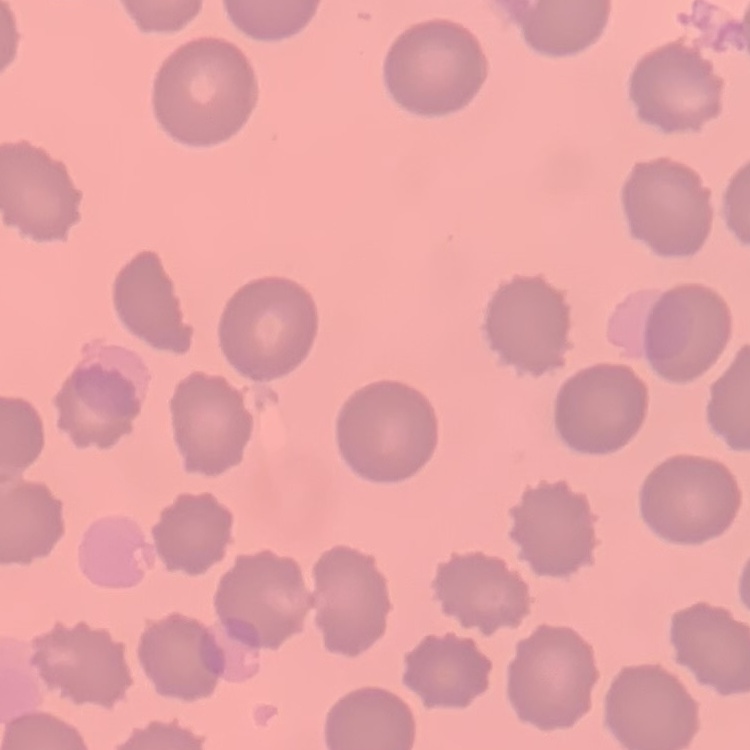
Summary:
  - Erythrocyte morphology: no rouleaux formation
  - Stain: Field's or Giemsa
  - Preparation: thin peripheral smear
  - Image type: square crop of a larger photomicrograph